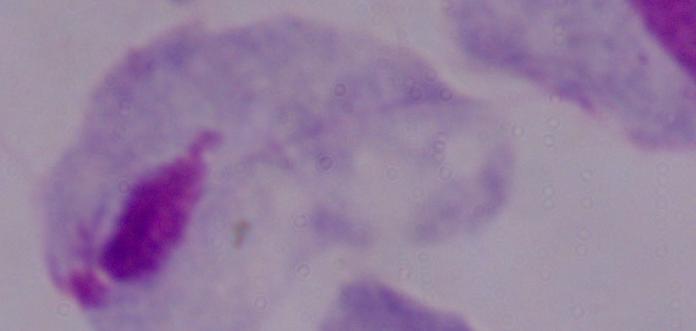
Micrograph. A trichomonad is shown. Captured at 1000x magnification.